Classify this cell by malaria status.
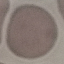
Uninfected.

Summary:
  - Preparation: thin blood smear
  - Stain: Giemsa
  - Capture: smartphone through the microscope eyepiece
  - Image type: cell patch, automatically extracted from a larger field of view and resized to 64 × 64 pixels